Describe the morphology of the erythrocytes.
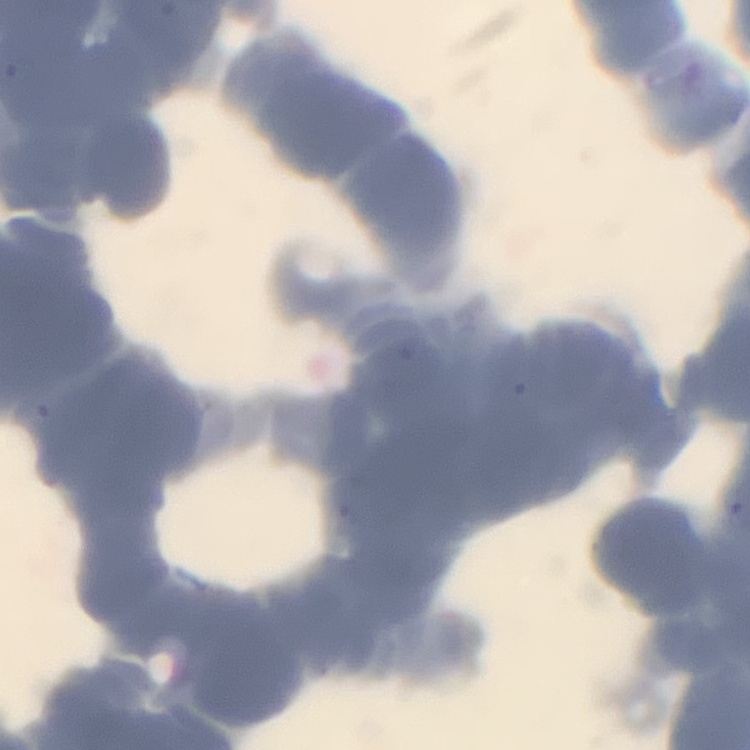

Rouleaux formation.

Summary:
  - Stain: Field's or Giemsa
  - Image type: one tile cut from a larger photomicrograph
  - Preparation: thin blood film